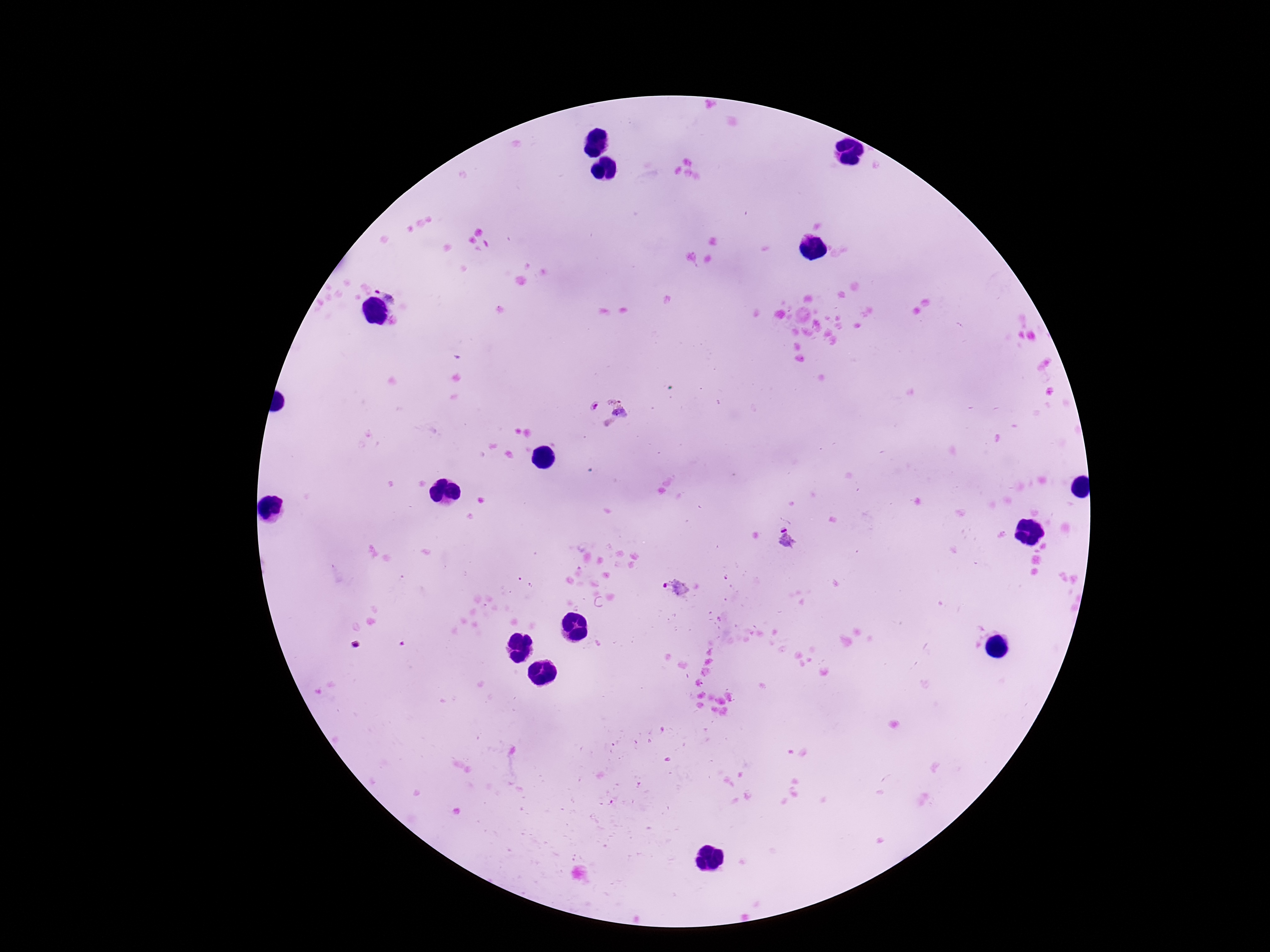

Approximate object centers, in pixels from the top-left corner. Plasmodium parasite locations: (x=389, y=289), (x=621, y=407), (x=785, y=538), (x=675, y=590). 100x magnification. Image is 1270×952 pixels. Thick blood film. Giemsa stain. One field from this slide. Patient malaria status: positive. Smartphone photograph taken through the microscope eyepiece.